Outline each blood parasite and name the species.
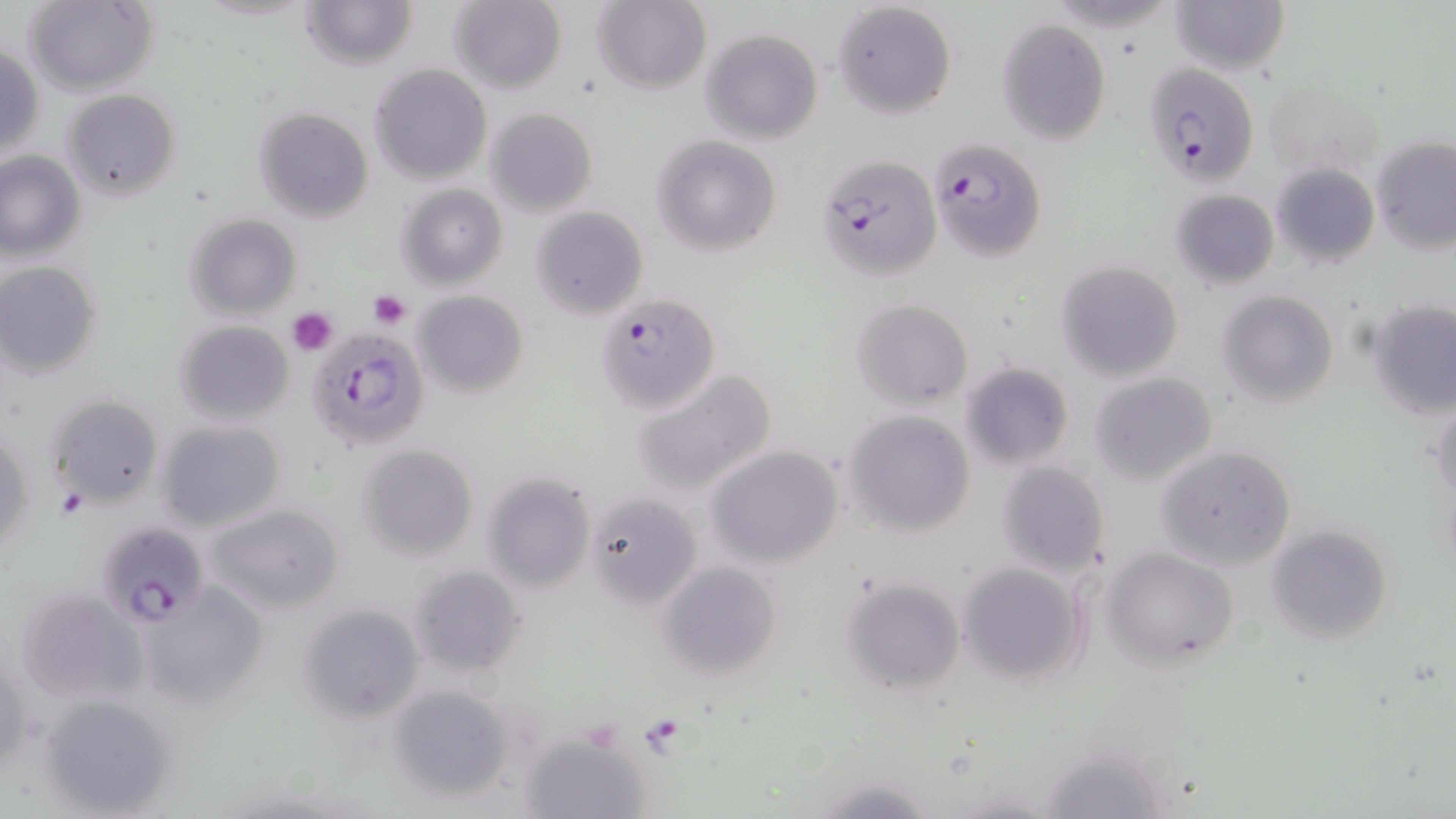
Approximate bounding boxes as [x1, y1, x2, y2] in pixels.
Plasmodium falciparum-infected red blood cells: [1142, 62, 1260, 186], [931, 137, 1045, 262], [815, 154, 941, 282], [598, 293, 725, 430], [306, 323, 432, 470], [95, 519, 212, 626].
No Plasmodium ovale, Plasmodium malariae, Plasmodium vivax, Babesia divergens, or Trypanosoma brucei observed.

Summary:
  - Uninfected red blood cell locations: [21, 0, 159, 96], [300, 0, 418, 71], [447, 0, 568, 96], [831, 0, 956, 119], [1169, 0, 1290, 76], [590, 1, 713, 95], [1041, 2, 1182, 33], [996, 17, 1114, 147], [699, 27, 824, 145], [1, 44, 45, 162], [368, 64, 492, 185], [1264, 72, 1386, 186], [62, 88, 182, 200], [253, 106, 375, 224], [484, 107, 598, 216], [651, 134, 782, 257], [1371, 136, 1456, 257], [0, 151, 85, 262], [1271, 161, 1380, 269], [396, 184, 508, 291], [1169, 189, 1279, 289], [531, 206, 649, 319], [183, 213, 302, 321], [0, 261, 103, 380], [1055, 261, 1184, 381], [414, 290, 528, 398], [1217, 290, 1341, 406], [850, 297, 974, 411], [1368, 299, 1456, 420], [173, 319, 294, 425], [958, 361, 1076, 468], [631, 367, 778, 497], [1087, 372, 1217, 485], [44, 393, 163, 507], [1429, 397, 1456, 508], [842, 409, 977, 536], [155, 419, 286, 533], [1, 426, 33, 557], [356, 444, 480, 561], [704, 445, 845, 569], [1156, 445, 1297, 570], [995, 460, 1113, 579], [479, 471, 595, 592], [585, 491, 701, 609], [204, 502, 345, 615], [1265, 524, 1393, 645], [1100, 545, 1239, 668], [657, 561, 782, 679], [955, 561, 1091, 688], [407, 565, 527, 679], [837, 574, 965, 695], [137, 582, 266, 707], [14, 588, 148, 708], [297, 602, 425, 723], [386, 685, 518, 805], [35, 692, 177, 817], [519, 732, 652, 819], [1038, 742, 1170, 819], [811, 774, 938, 818]
  - Platelet locations: [368, 290, 410, 329], [289, 307, 338, 355], [57, 486, 90, 520], [639, 715, 688, 755]
  - Slide-level diagnosis: Plasmodium falciparum
  - Preparation: thin blood smear
  - Field of view: one of a larger specimen
  - Stain: May-Grünwald-Giemsa
  - Modality: light microscopy
  - Image size: 1456×819 pixels
  - Magnification: 1000x